Outline each blood parasite and name the species.
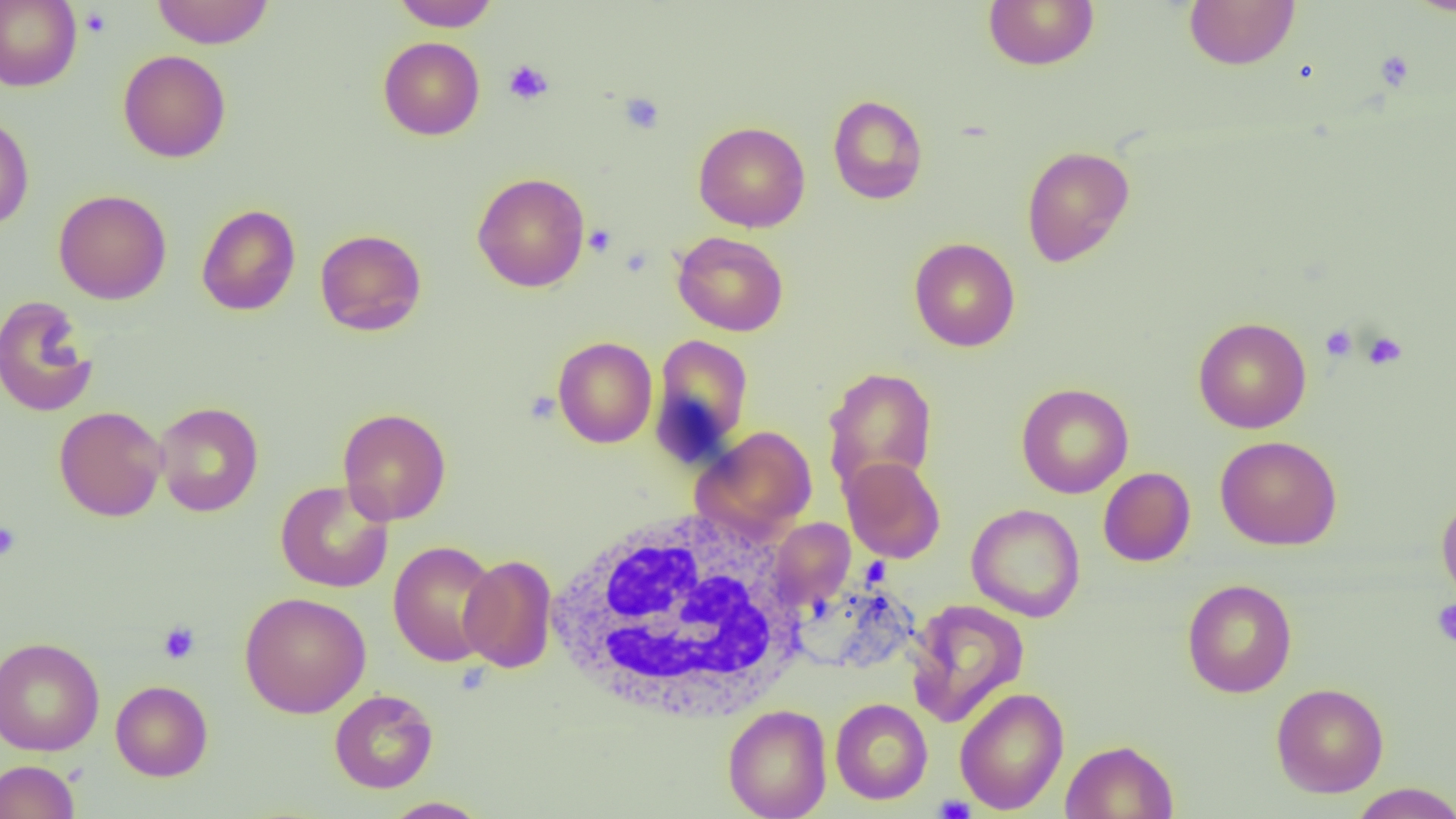

No blood parasites observed.

Approximate bounding boxes as named x1/y1/x2/y2 corners in pixels. White blood cell locations: (x1=541, y1=506, x2=812, y2=724). Uninfected red blood cell locations: (x1=0, y1=0, x2=82, y2=91), (x1=151, y1=0, x2=274, y2=49), (x1=391, y1=0, x2=499, y2=31), (x1=983, y1=0, x2=1099, y2=70), (x1=1183, y1=0, x2=1300, y2=70), (x1=1404, y1=0, x2=1456, y2=16), (x1=378, y1=36, x2=485, y2=140), (x1=118, y1=49, x2=231, y2=163), (x1=827, y1=94, x2=928, y2=204), (x1=0, y1=113, x2=34, y2=230), (x1=693, y1=121, x2=810, y2=232), (x1=1021, y1=145, x2=1135, y2=267), (x1=472, y1=172, x2=590, y2=292), (x1=53, y1=189, x2=171, y2=304), (x1=196, y1=204, x2=301, y2=316), (x1=315, y1=229, x2=427, y2=336), (x1=672, y1=231, x2=789, y2=336), (x1=909, y1=237, x2=1020, y2=352), (x1=0, y1=296, x2=98, y2=417), (x1=1193, y1=317, x2=1312, y2=433), (x1=652, y1=334, x2=755, y2=460), (x1=552, y1=336, x2=657, y2=448), (x1=822, y1=366, x2=938, y2=496), (x1=1016, y1=382, x2=1134, y2=498), (x1=153, y1=401, x2=264, y2=517), (x1=54, y1=406, x2=168, y2=521), (x1=337, y1=407, x2=451, y2=525), (x1=692, y1=425, x2=817, y2=539), (x1=1215, y1=435, x2=1342, y2=551), (x1=841, y1=457, x2=945, y2=563), (x1=1098, y1=467, x2=1195, y2=567), (x1=275, y1=480, x2=394, y2=593), (x1=1437, y1=494, x2=1456, y2=605), (x1=966, y1=503, x2=1085, y2=622), (x1=769, y1=518, x2=855, y2=610), (x1=388, y1=540, x2=501, y2=667), (x1=459, y1=554, x2=558, y2=673), (x1=1182, y1=579, x2=1297, y2=697), (x1=239, y1=591, x2=371, y2=718), (x1=906, y1=598, x2=1030, y2=728), (x1=1, y1=636, x2=104, y2=756), (x1=111, y1=680, x2=212, y2=781), (x1=1271, y1=682, x2=1389, y2=798), (x1=954, y1=687, x2=1069, y2=815), (x1=329, y1=689, x2=438, y2=793), (x1=830, y1=698, x2=933, y2=804), (x1=723, y1=704, x2=832, y2=819), (x1=1061, y1=739, x2=1178, y2=819), (x1=0, y1=759, x2=80, y2=819), (x1=1348, y1=783, x2=1456, y2=819), (x1=381, y1=797, x2=490, y2=818). Platelet locations: (x1=79, y1=6, x2=111, y2=38), (x1=1375, y1=51, x2=1415, y2=91), (x1=503, y1=60, x2=554, y2=105), (x1=619, y1=92, x2=664, y2=134), (x1=584, y1=224, x2=616, y2=256), (x1=1320, y1=325, x2=1357, y2=361), (x1=1362, y1=331, x2=1407, y2=370), (x1=524, y1=391, x2=560, y2=424), (x1=0, y1=521, x2=21, y2=562), (x1=1431, y1=599, x2=1456, y2=647), (x1=158, y1=621, x2=201, y2=664), (x1=934, y1=794, x2=976, y2=819). Slide-level diagnosis: negative for blood parasites. Optical microscopy. One field of a larger specimen. Image is 1456×819 pixels. Captured at 1000x magnification. Thin blood smear.